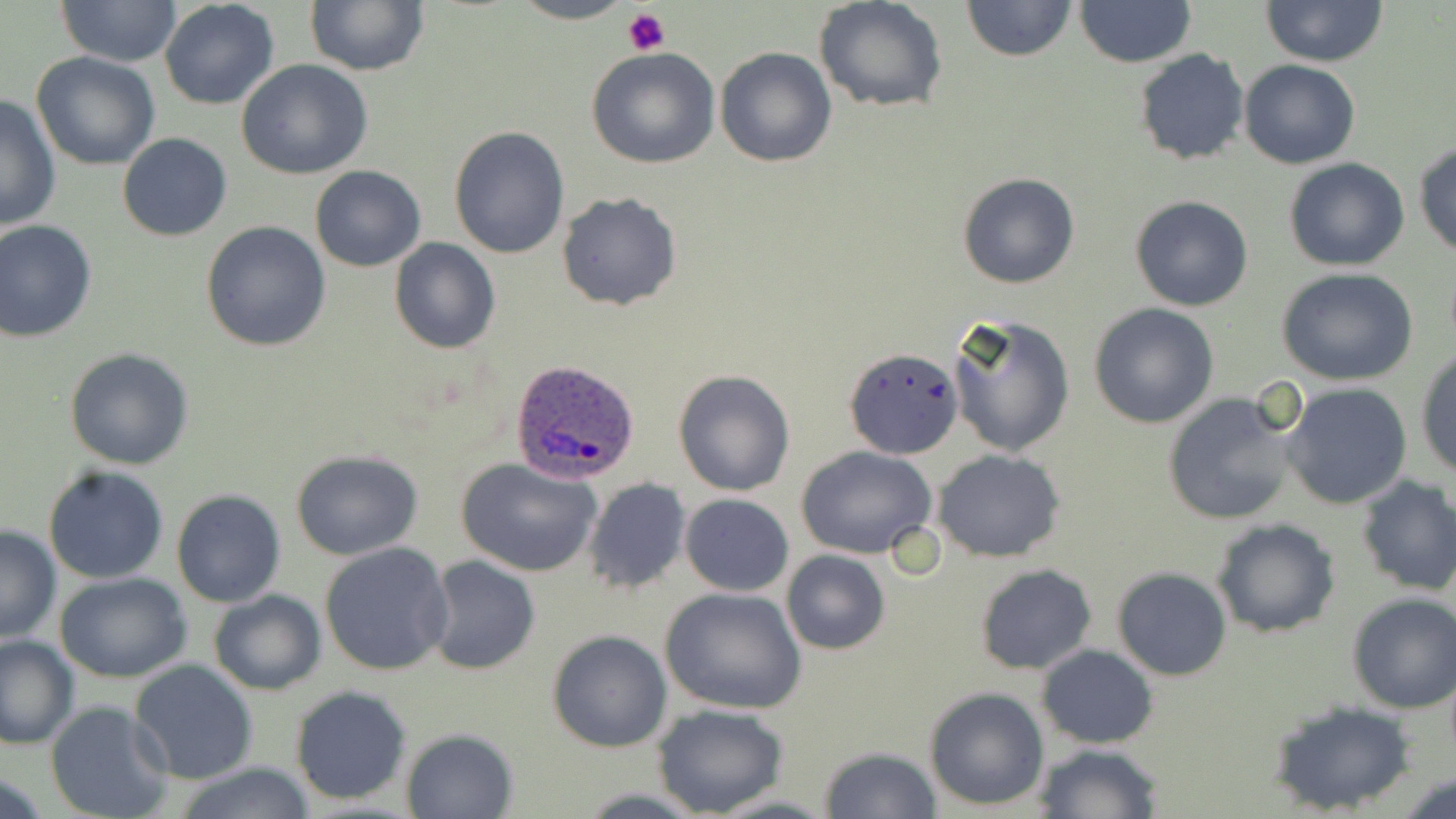 Approximate bounding boxes as named x1/y1/x2/y2 corners in pixels. Platelet locations: (x1=622, y1=10, x2=671, y2=55). Uninfected red blood cell locations: (x1=58, y1=0, x2=181, y2=68), (x1=508, y1=0, x2=637, y2=24), (x1=963, y1=0, x2=1074, y2=61), (x1=1073, y1=0, x2=1198, y2=67), (x1=1262, y1=0, x2=1389, y2=67), (x1=159, y1=1, x2=280, y2=110), (x1=305, y1=1, x2=429, y2=74), (x1=815, y1=1, x2=949, y2=114), (x1=715, y1=46, x2=836, y2=167), (x1=586, y1=47, x2=721, y2=169), (x1=1133, y1=48, x2=1252, y2=167), (x1=31, y1=52, x2=161, y2=171), (x1=236, y1=58, x2=372, y2=180), (x1=1239, y1=59, x2=1360, y2=168), (x1=1, y1=95, x2=60, y2=235), (x1=448, y1=127, x2=570, y2=260), (x1=117, y1=132, x2=232, y2=241), (x1=1414, y1=143, x2=1456, y2=258), (x1=1283, y1=158, x2=1410, y2=271), (x1=310, y1=165, x2=425, y2=272), (x1=958, y1=171, x2=1082, y2=290), (x1=556, y1=191, x2=683, y2=311), (x1=1129, y1=195, x2=1255, y2=313), (x1=0, y1=218, x2=97, y2=342), (x1=201, y1=222, x2=331, y2=352), (x1=389, y1=239, x2=501, y2=354), (x1=1276, y1=268, x2=1421, y2=387), (x1=1088, y1=303, x2=1220, y2=429), (x1=945, y1=310, x2=1076, y2=457), (x1=63, y1=347, x2=194, y2=470), (x1=1415, y1=349, x2=1456, y2=479), (x1=845, y1=350, x2=960, y2=461), (x1=673, y1=371, x2=794, y2=495), (x1=1279, y1=382, x2=1413, y2=510), (x1=1161, y1=392, x2=1298, y2=527), (x1=796, y1=445, x2=939, y2=561), (x1=290, y1=450, x2=423, y2=561), (x1=934, y1=450, x2=1064, y2=561), (x1=455, y1=456, x2=603, y2=576), (x1=42, y1=465, x2=170, y2=584), (x1=1352, y1=474, x2=1456, y2=597), (x1=581, y1=478, x2=693, y2=595), (x1=172, y1=489, x2=285, y2=607), (x1=679, y1=493, x2=794, y2=596), (x1=1212, y1=518, x2=1340, y2=639), (x1=0, y1=525, x2=61, y2=643), (x1=319, y1=542, x2=454, y2=676), (x1=781, y1=550, x2=889, y2=655), (x1=425, y1=556, x2=541, y2=675), (x1=975, y1=564, x2=1097, y2=676), (x1=1113, y1=567, x2=1232, y2=680), (x1=54, y1=571, x2=193, y2=683), (x1=660, y1=588, x2=808, y2=716), (x1=208, y1=589, x2=326, y2=694), (x1=1345, y1=593, x2=1456, y2=714), (x1=546, y1=630, x2=672, y2=752), (x1=0, y1=635, x2=80, y2=749), (x1=1037, y1=644, x2=1159, y2=748), (x1=128, y1=660, x2=258, y2=785), (x1=289, y1=686, x2=413, y2=805), (x1=924, y1=687, x2=1050, y2=810), (x1=48, y1=700, x2=175, y2=819), (x1=1266, y1=700, x2=1416, y2=815), (x1=651, y1=703, x2=790, y2=818), (x1=400, y1=728, x2=517, y2=818), (x1=1033, y1=742, x2=1162, y2=818), (x1=819, y1=746, x2=944, y2=818), (x1=168, y1=763, x2=321, y2=819), (x1=1396, y1=772, x2=1455, y2=819). Plasmodium ovale-infected red blood cell locations: (x1=509, y1=359, x2=637, y2=483). Slide-level diagnosis: Plasmodium ovale. Light microscopy. Thin blood smear. May-Grünwald-Giemsa stain. One field of a larger specimen. Image is 1456×819 pixels. Captured at 1000x magnification.